Mark where platelets are.
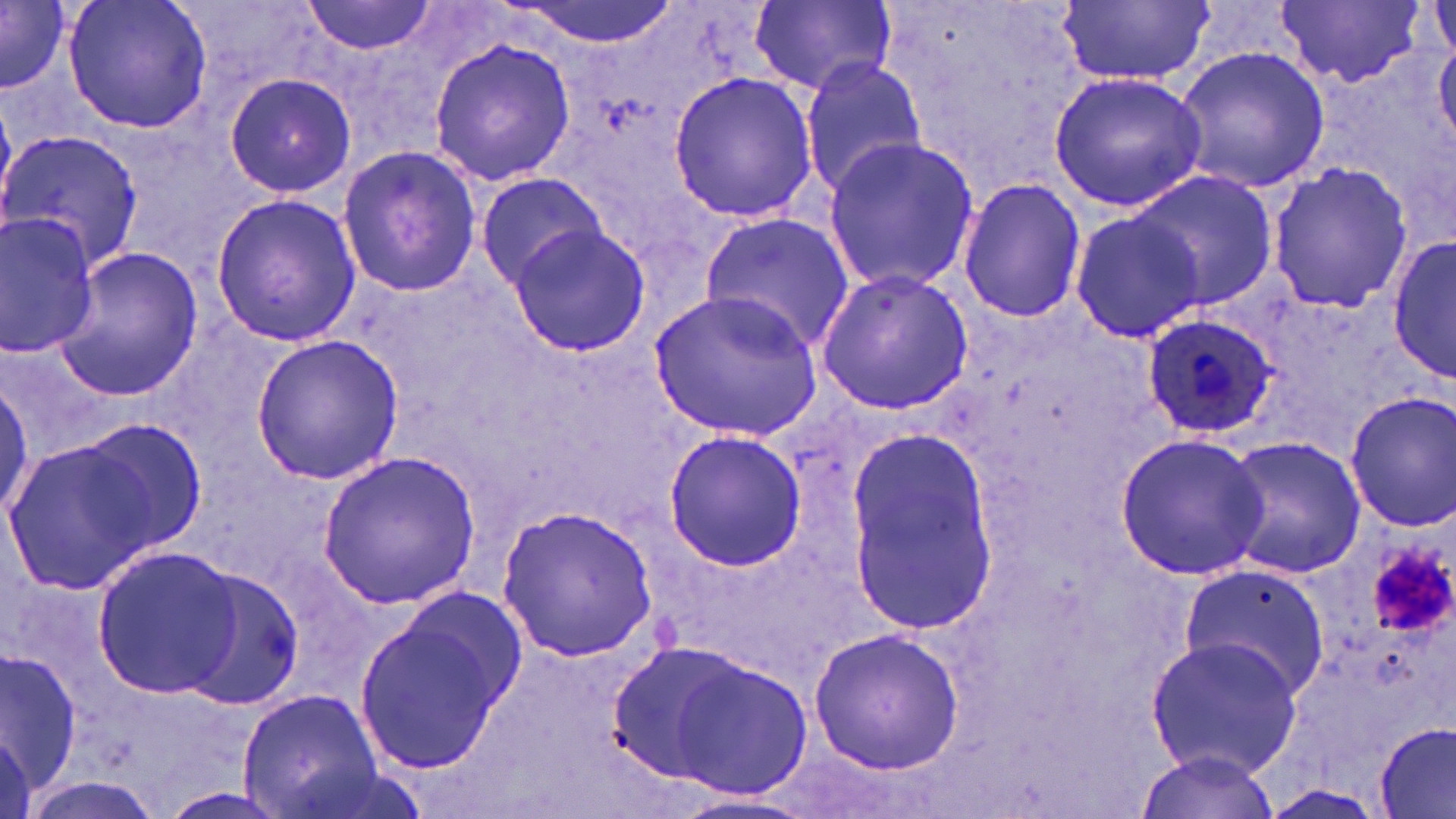

Approximate bounding boxes as [x1, y1, x2, y2] in pixels.
Platelets: [1366, 542, 1454, 639].

{
  "plasmodium_ovale_infected_red_blood_cell_locations": "approximate bounding boxes as [x1, y1, x2, y2] in pixels: [1141, 312, 1281, 441]",
  "slide_level_diagnosis": "Plasmodium ovale",
  "stain": "May-Grünwald-Giemsa",
  "image_size": "1456×819 pixels",
  "uninfected_red_blood_cell_locations": "approximate bounding boxes as [x1, y1, x2, y2] in pixels: [63, 0, 211, 134], [301, 0, 443, 56], [509, 0, 682, 47], [1277, 0, 1424, 87], [1427, 0, 1455, 72], [0, 1, 69, 94], [1059, 1, 1211, 87], [751, 2, 895, 94], [1434, 34, 1455, 150], [426, 36, 577, 186], [1172, 46, 1330, 193], [797, 57, 929, 195], [667, 70, 817, 223], [1048, 71, 1208, 213], [224, 72, 356, 199], [0, 129, 144, 273], [823, 137, 981, 294], [337, 145, 484, 297], [1266, 165, 1412, 309], [1125, 169, 1280, 310], [475, 173, 610, 287], [958, 177, 1085, 323], [209, 193, 361, 347], [1071, 210, 1204, 342], [0, 211, 103, 359], [699, 211, 855, 355], [507, 224, 652, 358], [1389, 232, 1456, 386], [53, 245, 202, 399], [814, 268, 974, 416], [648, 283, 824, 441], [249, 334, 405, 486], [0, 373, 32, 527], [1344, 390, 1455, 532], [71, 420, 209, 555], [662, 430, 807, 571], [842, 434, 999, 627], [1113, 434, 1267, 580], [1222, 435, 1366, 580], [3, 436, 163, 595], [315, 450, 481, 609], [495, 505, 658, 663], [90, 547, 242, 697], [1176, 562, 1329, 701], [172, 567, 305, 710], [353, 594, 520, 780], [809, 626, 964, 773], [1145, 637, 1302, 778], [2, 650, 83, 799], [667, 657, 810, 802], [237, 689, 383, 817], [1375, 721, 1456, 818], [0, 726, 32, 817], [1138, 749, 1281, 817], [672, 794, 820, 819]",
  "field_of_view": "single",
  "preparation": "thin blood smear",
  "modality": "optical microscopy",
  "magnification": "1000x"
}